Outline each blood parasite and name the species.
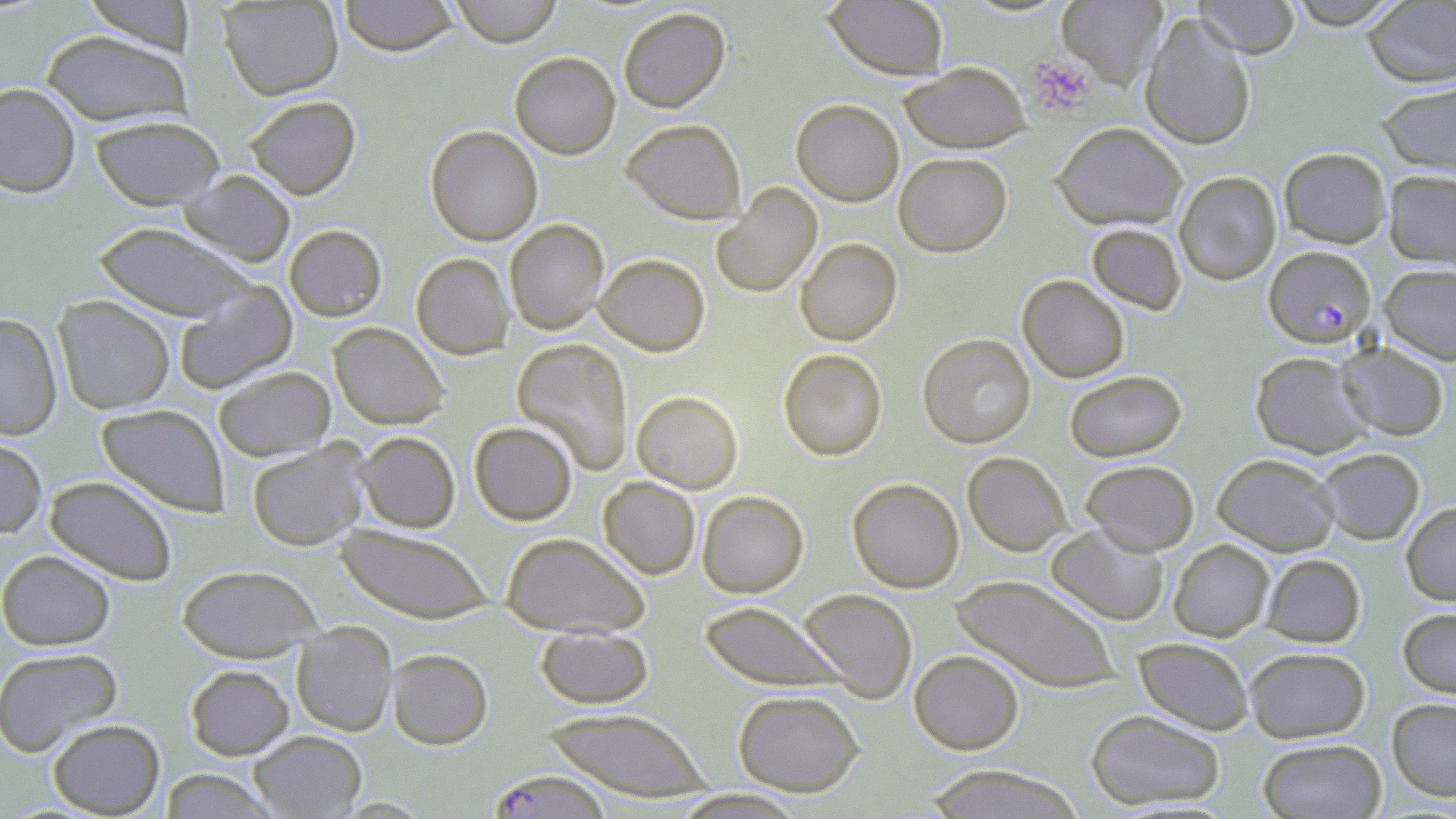
Approximate bounding boxes as (x1, y1, x2, y2) in pixels.
Plasmodium falciparum-infected red blood cells: (1264, 246, 1376, 347), (487, 770, 613, 819).
No Plasmodium ovale, Plasmodium malariae, Plasmodium vivax, Babesia divergens, or Trypanosoma brucei observed.

Platelet locations: (1026, 56, 1097, 117). Uninfected red blood cell locations: (81, 0, 197, 55), (337, 0, 459, 57), (448, 0, 564, 47), (1193, 0, 1302, 57), (1283, 0, 1407, 29), (217, 1, 344, 100), (822, 1, 951, 81), (1056, 1, 1167, 90), (1361, 1, 1456, 87), (617, 7, 731, 113), (1139, 12, 1256, 150), (40, 30, 193, 128), (509, 52, 621, 159), (899, 61, 1031, 153), (1375, 79, 1456, 180), (0, 83, 81, 198), (244, 95, 361, 200), (790, 98, 904, 206), (90, 115, 225, 211), (622, 117, 746, 222), (1052, 122, 1188, 231), (425, 125, 543, 246), (1278, 147, 1391, 248), (894, 152, 1012, 256), (179, 170, 296, 267), (1384, 170, 1456, 268), (1173, 171, 1282, 286), (711, 183, 822, 298), (504, 219, 609, 335), (91, 222, 255, 322), (1086, 223, 1186, 315), (284, 224, 387, 322), (794, 237, 902, 345), (410, 252, 514, 359), (594, 253, 710, 356), (1379, 263, 1456, 365), (1017, 275, 1130, 383), (173, 280, 297, 394), (53, 296, 175, 414), (0, 313, 63, 440), (329, 322, 450, 429), (918, 333, 1035, 449), (511, 339, 634, 474), (1336, 341, 1450, 441), (778, 348, 887, 461), (1249, 351, 1372, 458), (213, 365, 335, 460), (1064, 370, 1186, 461), (631, 391, 743, 493), (96, 404, 230, 517), (469, 421, 578, 525), (354, 431, 461, 533), (0, 437, 48, 538), (246, 441, 371, 551), (1315, 447, 1425, 545), (963, 451, 1072, 556), (1212, 452, 1341, 555), (1080, 459, 1199, 554), (44, 475, 178, 586), (598, 477, 701, 579), (847, 477, 964, 593), (697, 491, 809, 598), (1401, 501, 1456, 606), (335, 523, 494, 624), (1046, 524, 1169, 626), (500, 532, 650, 636), (1168, 539, 1274, 642), (0, 550, 116, 650), (1261, 553, 1366, 648), (177, 564, 323, 661), (949, 574, 1122, 693), (798, 588, 918, 703), (699, 601, 848, 692), (1397, 607, 1456, 698), (291, 623, 397, 737), (535, 626, 654, 709), (1133, 637, 1254, 734), (1244, 646, 1371, 743), (0, 647, 124, 757), (386, 648, 494, 750), (909, 650, 1025, 754), (185, 664, 294, 760), (732, 690, 866, 797), (1387, 698, 1456, 801), (540, 707, 715, 801), (1085, 708, 1226, 810), (47, 718, 165, 817), (249, 730, 366, 818), (1257, 738, 1387, 818), (921, 765, 1088, 818), (158, 768, 281, 818), (669, 789, 811, 818). Slide-level diagnosis: Plasmodium falciparum. Optical microscopy. Thin blood smear. Captured at 1000x magnification. One field of a larger specimen. Image is 1456×819 pixels. May-Grünwald-Giemsa-stained preparation.